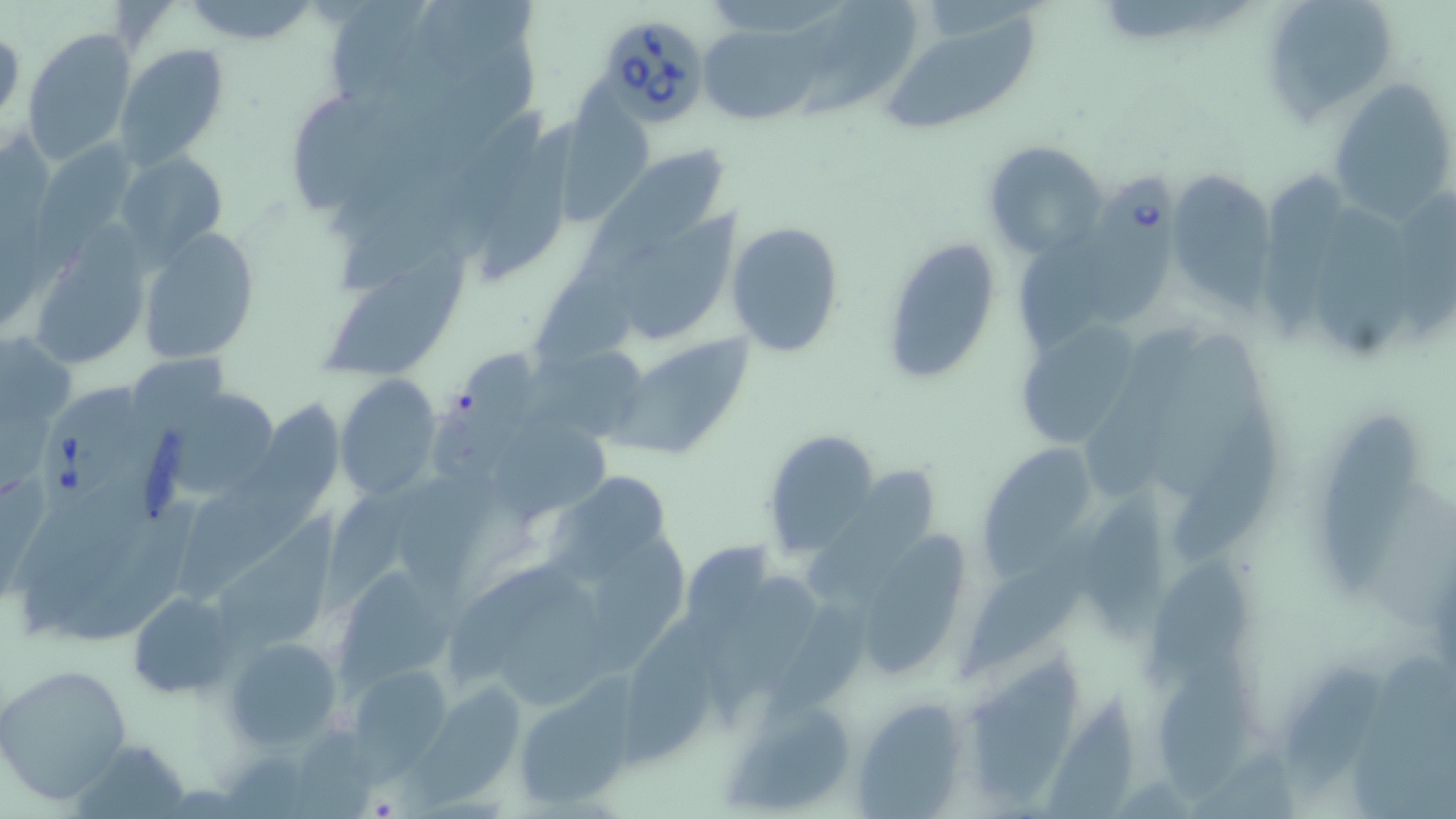

Approximate bounding boxes as named x1/y1/x2/y2 corners in pixels. Uninfected red blood cell locations: (x1=416, y1=0, x2=544, y2=68), (x1=1261, y1=0, x2=1398, y2=122), (x1=183, y1=1, x2=318, y2=45), (x1=808, y1=1, x2=916, y2=118), (x1=878, y1=15, x2=1043, y2=138), (x1=697, y1=24, x2=825, y2=126), (x1=21, y1=27, x2=138, y2=164), (x1=114, y1=43, x2=229, y2=171), (x1=560, y1=79, x2=661, y2=231), (x1=1325, y1=79, x2=1456, y2=220), (x1=481, y1=118, x2=591, y2=277), (x1=982, y1=141, x2=1106, y2=258), (x1=582, y1=147, x2=732, y2=284), (x1=114, y1=150, x2=226, y2=260), (x1=1255, y1=158, x2=1355, y2=350), (x1=1167, y1=169, x2=1277, y2=310), (x1=611, y1=200, x2=755, y2=349), (x1=1312, y1=202, x2=1422, y2=362), (x1=728, y1=223, x2=846, y2=358), (x1=28, y1=229, x2=154, y2=372), (x1=140, y1=229, x2=259, y2=361), (x1=881, y1=237, x2=998, y2=382), (x1=315, y1=263, x2=468, y2=374), (x1=1016, y1=322, x2=1141, y2=445), (x1=0, y1=330, x2=76, y2=435), (x1=606, y1=337, x2=755, y2=459), (x1=421, y1=342, x2=544, y2=488), (x1=520, y1=343, x2=654, y2=437), (x1=335, y1=376, x2=443, y2=501), (x1=168, y1=394, x2=292, y2=497), (x1=251, y1=398, x2=346, y2=515), (x1=1168, y1=409, x2=1280, y2=559), (x1=1321, y1=409, x2=1418, y2=601), (x1=500, y1=419, x2=623, y2=528), (x1=760, y1=430, x2=881, y2=555), (x1=981, y1=444, x2=1109, y2=578), (x1=172, y1=460, x2=336, y2=601), (x1=811, y1=468, x2=944, y2=601), (x1=546, y1=469, x2=678, y2=586), (x1=316, y1=471, x2=456, y2=625), (x1=13, y1=482, x2=157, y2=637), (x1=1085, y1=484, x2=1181, y2=645), (x1=961, y1=521, x2=1110, y2=674), (x1=861, y1=528, x2=971, y2=680), (x1=591, y1=533, x2=697, y2=664), (x1=1149, y1=554, x2=1255, y2=685), (x1=335, y1=556, x2=460, y2=688), (x1=716, y1=570, x2=826, y2=711), (x1=493, y1=586, x2=629, y2=702), (x1=127, y1=591, x2=234, y2=698), (x1=767, y1=596, x2=892, y2=719), (x1=614, y1=614, x2=735, y2=767), (x1=223, y1=637, x2=342, y2=752), (x1=1351, y1=643, x2=1456, y2=819), (x1=965, y1=646, x2=1079, y2=811), (x1=1275, y1=661, x2=1401, y2=796), (x1=1157, y1=662, x2=1264, y2=799), (x1=1, y1=664, x2=132, y2=804), (x1=348, y1=666, x2=452, y2=766), (x1=399, y1=685, x2=535, y2=803), (x1=513, y1=686, x2=629, y2=808), (x1=853, y1=695, x2=971, y2=815), (x1=727, y1=702, x2=853, y2=814). Babesia divergens-infected red blood cell locations: (x1=590, y1=11, x2=712, y2=124), (x1=1079, y1=160, x2=1186, y2=331), (x1=33, y1=380, x2=143, y2=508). Slide-level diagnosis: Babesia divergens. Single field of view. May-Grünwald-Giemsa-stained preparation. Light microscopy. Thin blood film. Captured at 1000x magnification. Image is 1456×819 pixels.